Describe the morphology of the erythrocytes.
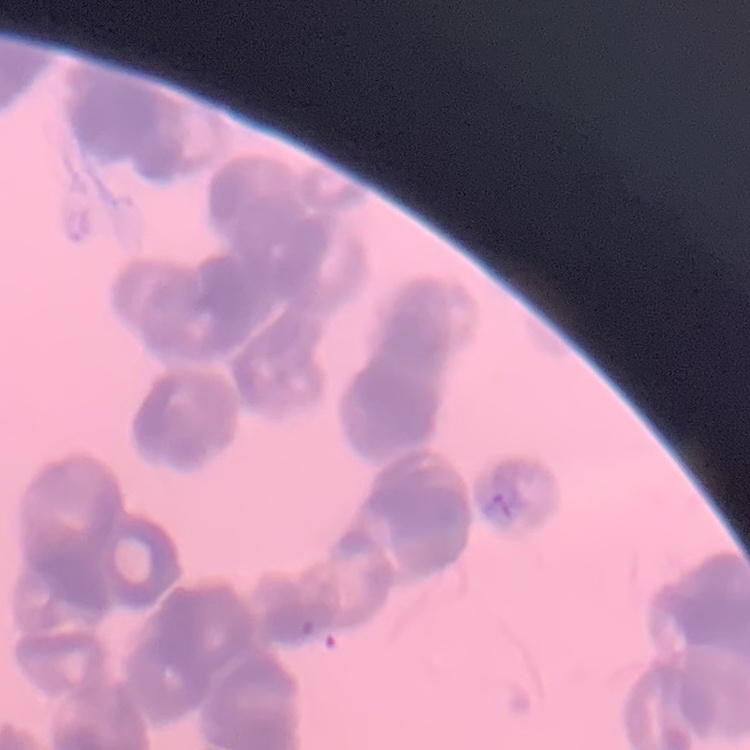
Rouleaux formation.

Summary:
  - Preparation: thin blood film
  - Image type: square crop of a larger photomicrograph
  - Stain: Field's or Giemsa